Report the malaria status of this cell.
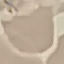

It is uninfected.

Summary:
  - Stain: Giemsa
  - Capture: smartphone through the microscope eyepiece
  - Preparation: thin blood smear
  - Image type: cell patch, automatically extracted from a larger field of view and resized to 64 × 64 pixels